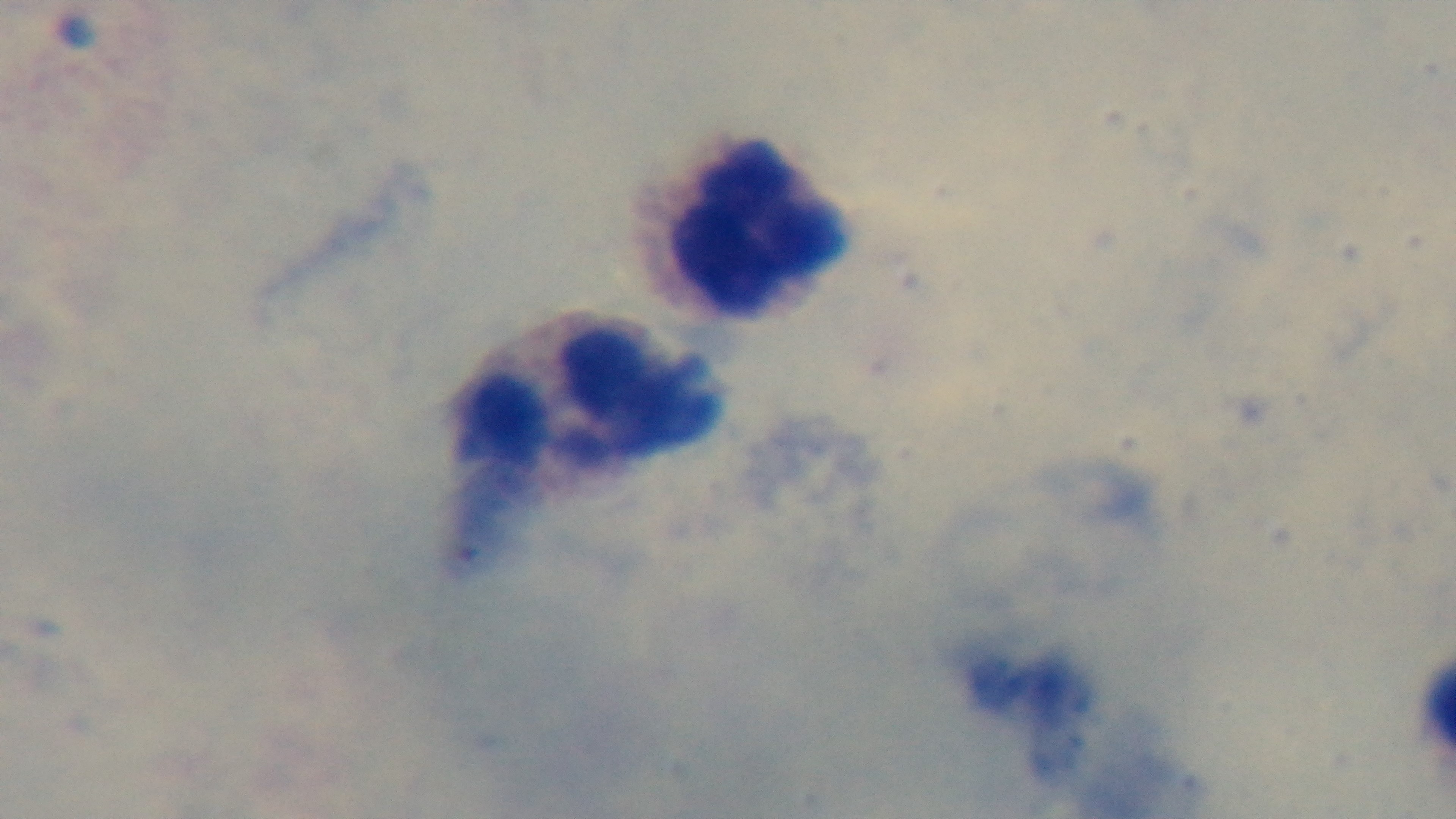
Summary:
  - Stain: Giemsa
  - Modality: light microscopy
  - Preparation: thick blood film
  - Capture: mounted 4K digital camera
  - Malaria status: uninfected
  - Field of view: one from the slide
  - Objective: 100x oil immersion